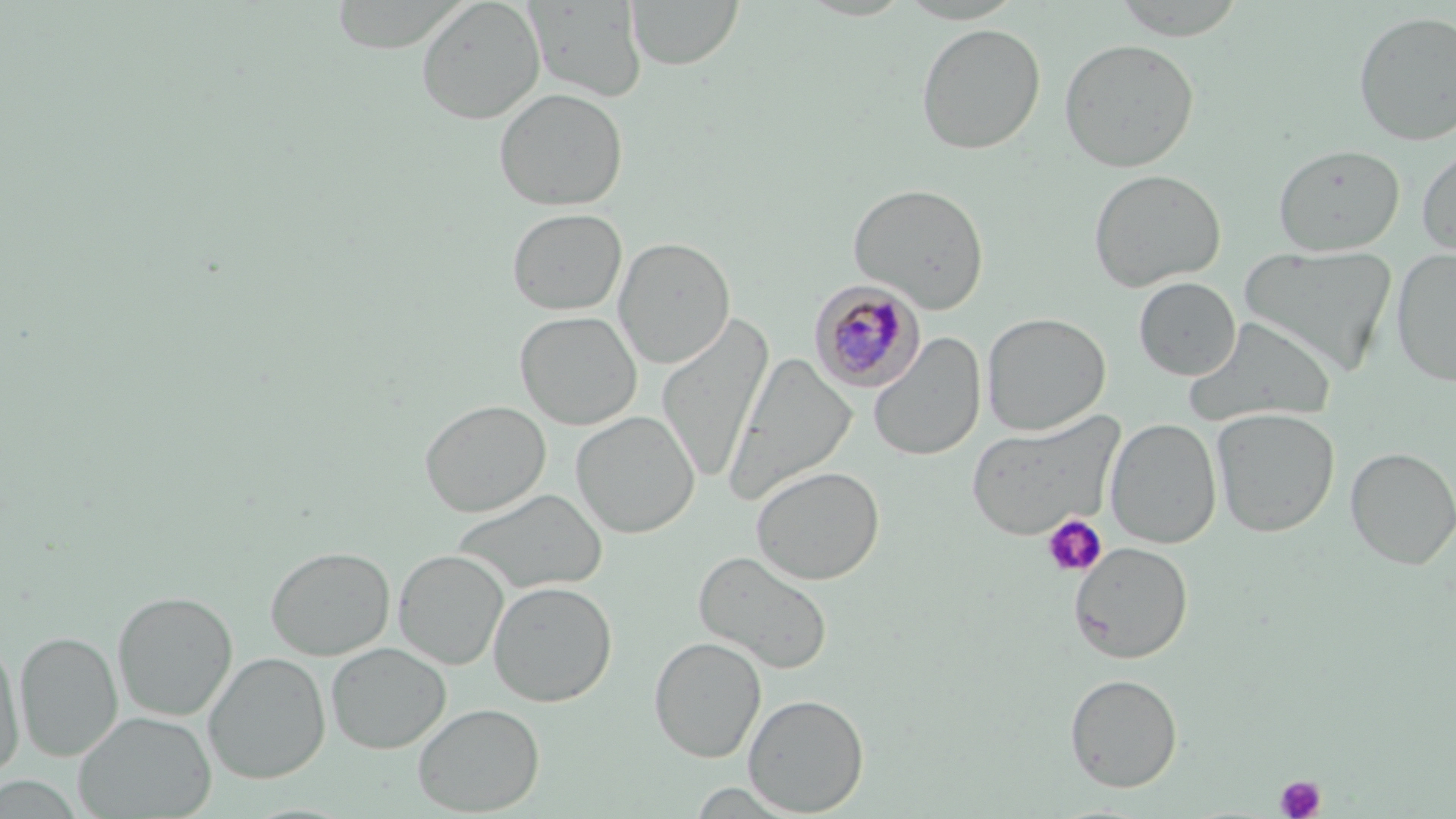
slide-level diagnosis = Plasmodium malariae
stain = May-Grünwald-Giemsa
uninfected red blood cell locations = approximate bounding boxes as (x1, y1, x2, y2) in pixels: (416, 0, 545, 124), (627, 0, 743, 70), (1109, 0, 1249, 40), (525, 1, 647, 103), (1353, 10, 1456, 147), (915, 23, 1046, 154), (1058, 38, 1200, 172), (493, 88, 628, 211), (1416, 140, 1456, 257), (1273, 143, 1406, 256), (1088, 168, 1226, 292), (848, 182, 989, 313), (506, 208, 627, 315), (614, 237, 736, 368), (1240, 245, 1398, 376), (1391, 248, 1456, 388), (1134, 277, 1241, 380), (514, 311, 641, 430), (981, 312, 1111, 436), (656, 314, 774, 485), (1184, 316, 1337, 427), (869, 327, 1108, 447), (868, 333, 986, 462), (724, 353, 857, 503), (420, 399, 550, 517), (1211, 407, 1340, 537), (571, 410, 700, 538), (965, 412, 1124, 542), (1105, 418, 1222, 549), (1345, 447, 1456, 569), (750, 465, 885, 585), (450, 488, 608, 596), (1069, 541, 1193, 663), (265, 545, 395, 661), (393, 549, 509, 670), (693, 549, 833, 675), (488, 580, 617, 707), (112, 590, 238, 721), (14, 630, 122, 762), (649, 636, 766, 762), (0, 637, 24, 777), (326, 642, 451, 753), (204, 651, 331, 784), (1064, 673, 1183, 792), (743, 693, 869, 816), (412, 703, 545, 815), (73, 711, 216, 818), (0, 773, 84, 818)
modality = optical microscopy
platelet locations = approximate bounding boxes as (x1, y1, x2, y2) in pixels: (1042, 514, 1107, 578), (1275, 774, 1326, 818)
field of view = single
Plasmodium malariae-infected red blood cell locations = approximate bounding boxes as (x1, y1, x2, y2) in pixels: (810, 280, 925, 393)
image size = 1456×819 pixels
preparation = thin blood film
magnification = 1000x